Assess this cell for malaria.
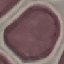
Uninfected.

stain = Giemsa
preparation = thin smear
image type = automatically extracted cell patch, resized to 64 × 64 pixels
capture = smartphone through the microscope eyepiece